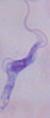

A trypanosome is shown. 1000x magnification. Photomicrograph.